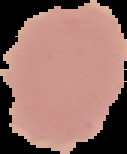 Image is 127×154 pixels. From a thin blood film. Result: no malaria parasites seen. Segmented cell region on a black background.